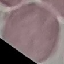 Result: no malaria parasites seen. Photographed with a smartphone camera at the microscope eyepiece. Giemsa stain. Automatically extracted cell patch, resized to 64 × 64 pixels. Thin blood smear.